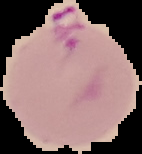
Summary:
  - Image type: segmented cell region with the area outside set to black
  - Preparation: thin blood smear
  - Image size: 142×154 pixels
  - Malaria status: parasitized